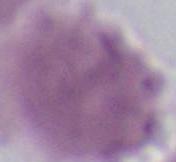
identification = erythrocyte
modality = photomicrograph
magnification = 1000x